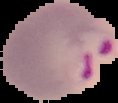

Image is 118×103 pixels. Segmented cell region on a black background. From a thin blood smear. Malaria status: parasitized.